State which cell type is depicted.
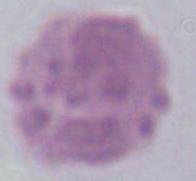
An erythrocyte.

1000x magnification. Photomicrograph.